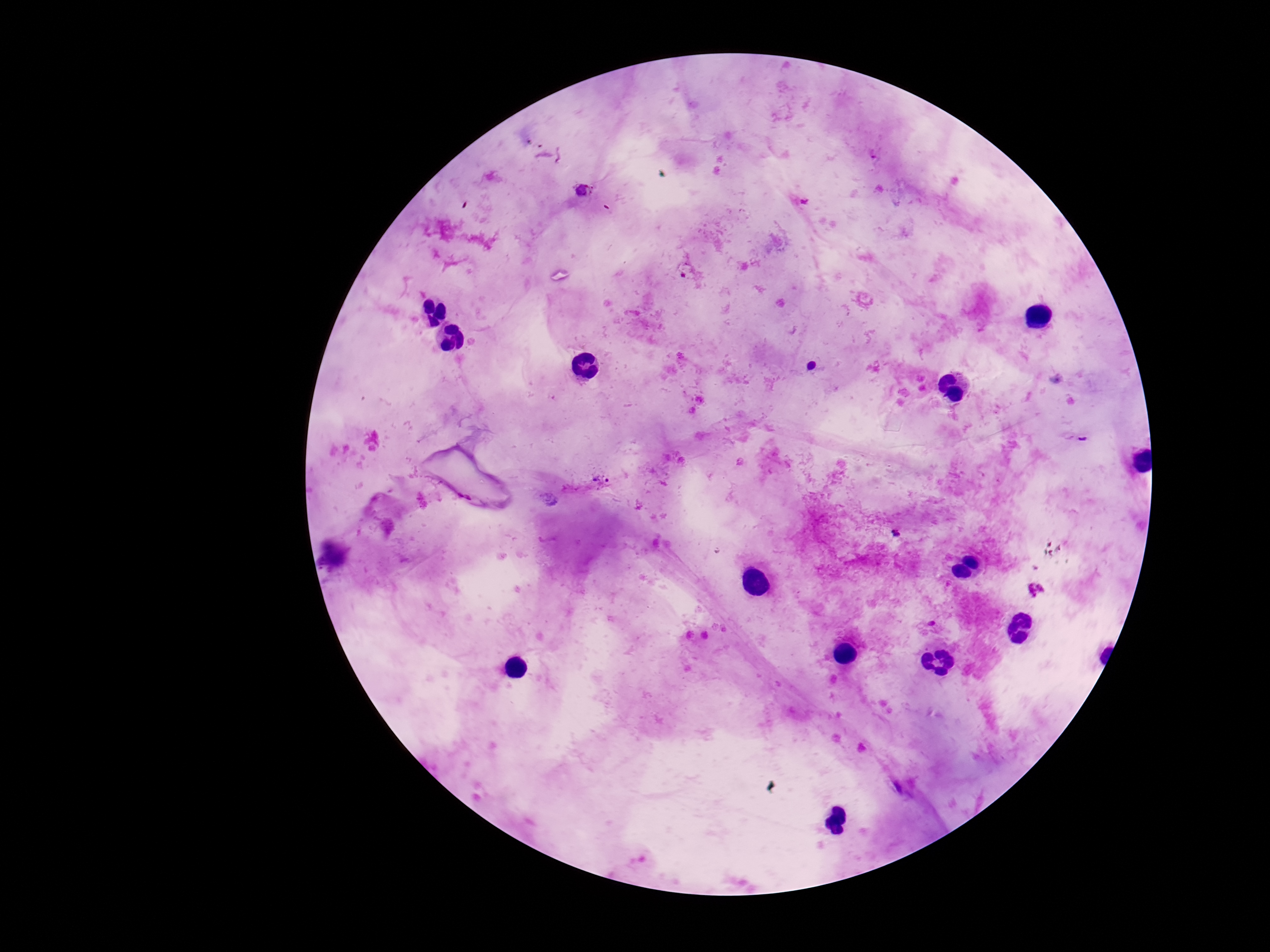 Approximate centers as [x, y] in pixels. Plasmodium parasite locations: [584, 190], [601, 479], [1036, 590]. Image is 1270×952 pixels. Thick blood film. Giemsa stain. Smartphone photograph taken through the microscope eyepiece. Patient malaria status: infected. 100x magnification. Single field of view.